Assess this cell for malaria.
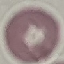

Uninfected.

Acquired by smartphone through the microscope eyepiece. Thin smear of blood. Giemsa stain. Automatically extracted cell patch, resized to 64 × 64 pixels.